Report the malaria status of this cell.
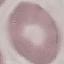
It is uninfected.

preparation = thin smear
capture = smartphone camera at the microscope eyepiece
image type = cell patch, automatically extracted from a larger field of view and resized to 64 × 64 pixels
stain = Giemsa